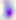

magnification = 400x
modality = photomicrograph
identification = Toxoplasma gondii